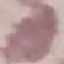
{
  "malaria_status": "uninfected",
  "preparation": "thin blood film",
  "stain": "Giemsa",
  "capture": "smartphone camera at the microscope eyepiece",
  "image_type": "automatically extracted cell patch, resized to 64 × 64 pixels"
}